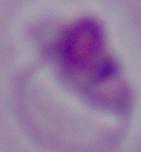
Summary:
  - Magnification: 1000x
  - Identification: Leishmania
  - Modality: micrograph